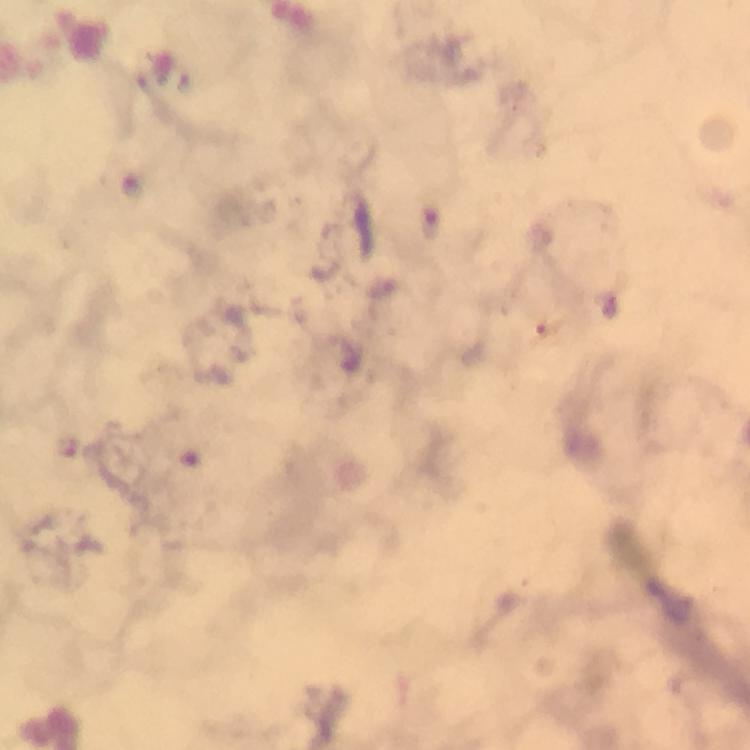

Approximate centers as (x, y) in pixels. Malaria parasite locations: (430, 222). A crop from one field of view. At 100x magnification. Thick blood smear. Image is 750×750 pixels. Giemsa-stained preparation. Immersion oil applied. From a diagnostic examination for malaria. Smartphone photograph taken through a microscope.